Assess this cell for malaria.
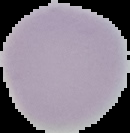

It is uninfected.

Image is 130×133 pixels. From a thin blood smear. Segmented cell region on a black background.